Assess this cell for malaria.
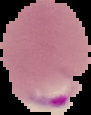

It is parasitized.

Image is 91×115 pixels. From a thin blood film. The area outside the segmented cell region is set to black.